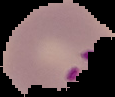

image size = 115×97 pixels
image type = segmented cell region on a black background
preparation = thin blood smear
malaria status = parasitized